Give the position of every Plasmodium falciparum parasite, noting its life-cycle stage.
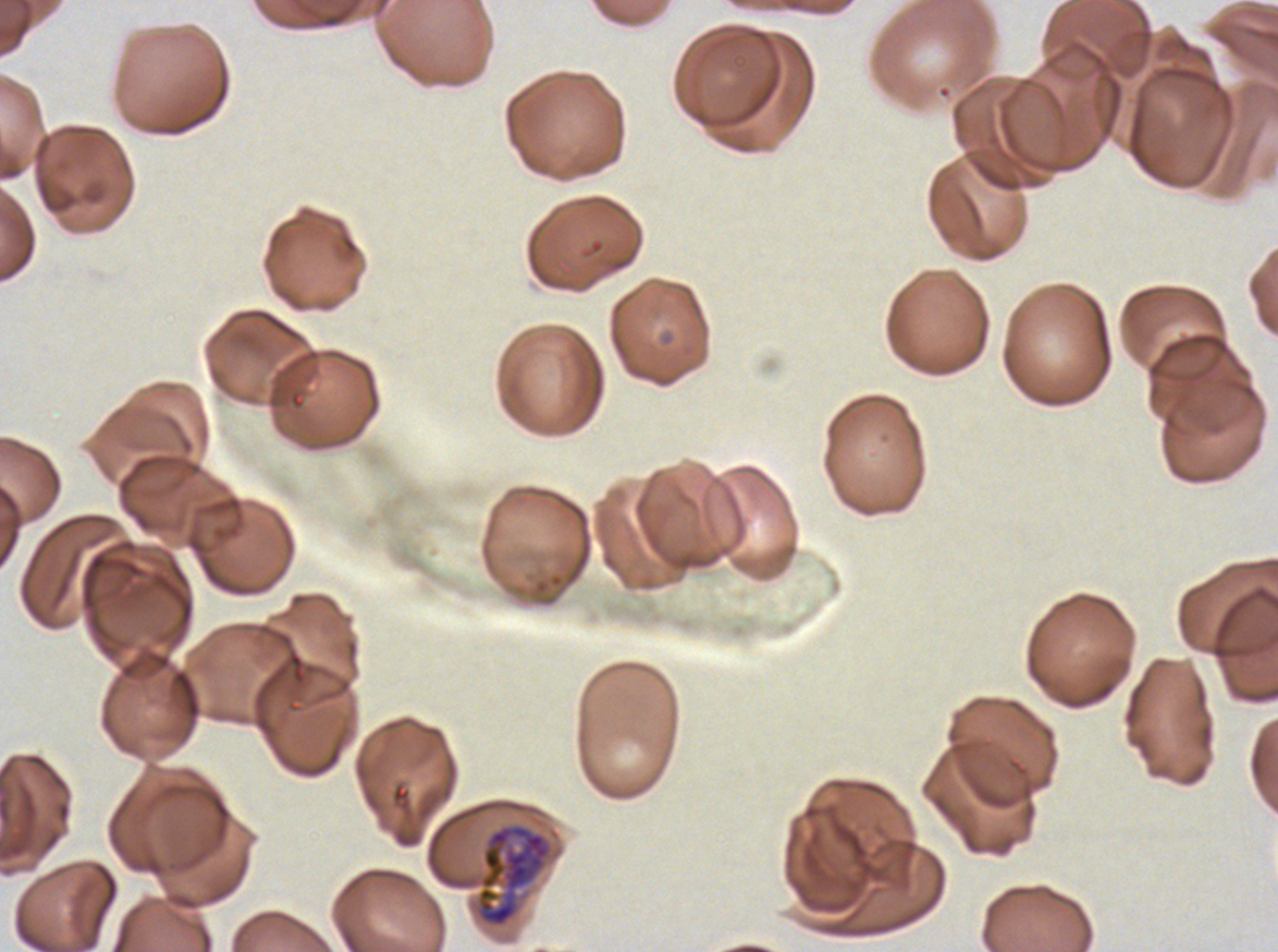

Approximate bounding boxes as {x1, y1, x2, y2} in pixels.
Late trophozoites: {476, 824, 552, 927}.
No rings, late-ring/early-trophozoite forms, mid trophozoites, early schizonts, late schizonts, segmenters, or gametocytes observed.

Image is 1278×952 pixels. Thin blood film. Giemsa-stained preparation. One sub-image of a larger composite. Plasmodium falciparum from a patient in The Gambia, cultured ex vivo for 24 to 48 hours.